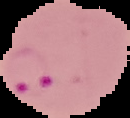

preparation = thin blood smear
image type = cell region segmented out of the field of view; surrounding area masked to black
result = Plasmodium parasites identified
image size = 130×118 pixels